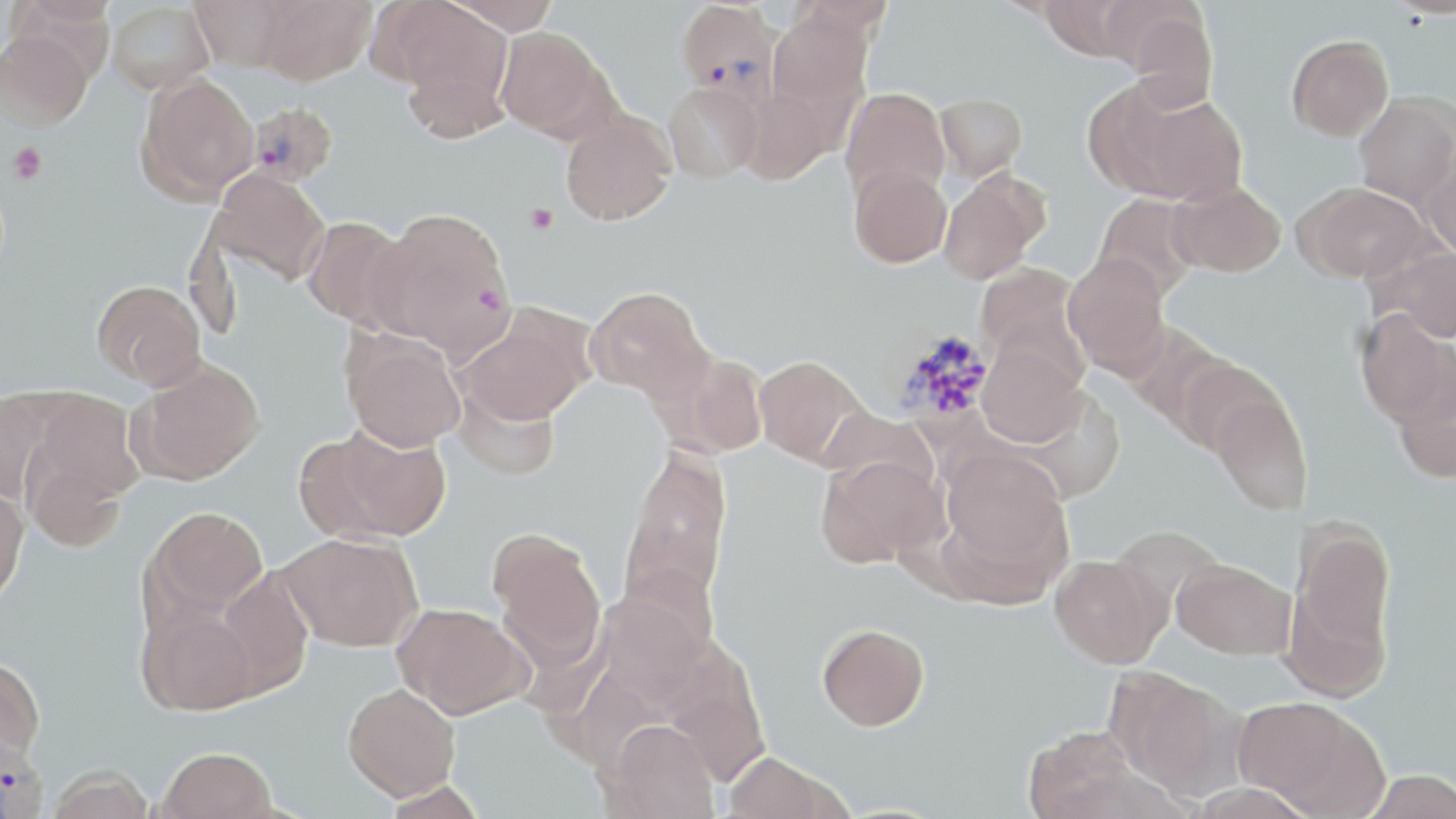
slide_level_diagnosis: Plasmodium vivax
platelet_locations: 'approximate bounding boxes as named x1/y1/x2/y2 corners in pixels: (x1=7, y1=142, x2=47, y2=183), (x1=525, y1=204, x2=558, y2=234)'
magnification: 1000x
plasmodium_vivax_infected_red_blood_cell_locations: 'approximate bounding boxes as named x1/y1/x2/y2 corners in pixels: (x1=676, y1=0, x2=783, y2=101), (x1=246, y1=102, x2=340, y2=187), (x1=886, y1=327, x2=995, y2=431), (x1=0, y1=731, x2=48, y2=818)'
uninfected_red_blood_cell_locations: 'approximate bounding boxes as named x1/y1/x2/y2 corners in pixels: (x1=190, y1=0, x2=295, y2=71), (x1=256, y1=0, x2=376, y2=84), (x1=440, y1=0, x2=560, y2=35), (x1=789, y1=0, x2=895, y2=36), (x1=1038, y1=0, x2=1142, y2=59), (x1=106, y1=2, x2=215, y2=95), (x1=384, y1=2, x2=514, y2=129), (x1=767, y1=5, x2=874, y2=122), (x1=1118, y1=9, x2=1218, y2=111), (x1=494, y1=27, x2=612, y2=139), (x1=0, y1=31, x2=94, y2=130), (x1=1287, y1=35, x2=1393, y2=141), (x1=135, y1=71, x2=260, y2=203), (x1=664, y1=81, x2=764, y2=183), (x1=1095, y1=81, x2=1247, y2=205), (x1=735, y1=87, x2=833, y2=185), (x1=840, y1=88, x2=950, y2=200), (x1=935, y1=93, x2=1027, y2=183), (x1=1354, y1=94, x2=1456, y2=208), (x1=560, y1=110, x2=676, y2=225), (x1=1419, y1=149, x2=1456, y2=259), (x1=849, y1=164, x2=951, y2=268), (x1=208, y1=167, x2=330, y2=286), (x1=938, y1=169, x2=1047, y2=285), (x1=1168, y1=180, x2=1286, y2=277), (x1=1298, y1=182, x2=1428, y2=282), (x1=1092, y1=193, x2=1203, y2=300), (x1=369, y1=207, x2=515, y2=358), (x1=300, y1=216, x2=412, y2=330), (x1=1374, y1=245, x2=1456, y2=342), (x1=1063, y1=253, x2=1172, y2=380), (x1=976, y1=262, x2=1089, y2=373), (x1=92, y1=279, x2=206, y2=390), (x1=585, y1=286, x2=711, y2=401), (x1=457, y1=307, x2=594, y2=425), (x1=1354, y1=309, x2=1454, y2=426), (x1=341, y1=328, x2=465, y2=451), (x1=977, y1=343, x2=1087, y2=448), (x1=658, y1=350, x2=769, y2=458), (x1=754, y1=355, x2=867, y2=466), (x1=132, y1=358, x2=266, y2=485), (x1=1174, y1=358, x2=1284, y2=457), (x1=1393, y1=366, x2=1456, y2=483), (x1=453, y1=380, x2=561, y2=481), (x1=1209, y1=388, x2=1313, y2=515), (x1=0, y1=390, x2=59, y2=504), (x1=22, y1=390, x2=144, y2=516), (x1=820, y1=407, x2=937, y2=495), (x1=299, y1=421, x2=451, y2=544), (x1=22, y1=441, x2=129, y2=553), (x1=620, y1=446, x2=733, y2=614), (x1=936, y1=447, x2=1072, y2=593), (x1=816, y1=454, x2=945, y2=568), (x1=0, y1=485, x2=29, y2=610), (x1=144, y1=506, x2=269, y2=624), (x1=1288, y1=521, x2=1396, y2=681), (x1=490, y1=529, x2=606, y2=672), (x1=278, y1=532, x2=422, y2=651), (x1=1049, y1=554, x2=1167, y2=668), (x1=1172, y1=559, x2=1295, y2=659), (x1=212, y1=568, x2=315, y2=699), (x1=590, y1=589, x2=708, y2=710), (x1=393, y1=603, x2=533, y2=719), (x1=138, y1=605, x2=259, y2=714), (x1=817, y1=623, x2=930, y2=731), (x1=659, y1=640, x2=771, y2=787), (x1=0, y1=655, x2=46, y2=765), (x1=1104, y1=667, x2=1242, y2=799), (x1=342, y1=683, x2=460, y2=801), (x1=1231, y1=696, x2=1376, y2=814), (x1=602, y1=719, x2=720, y2=819), (x1=1024, y1=725, x2=1146, y2=819), (x1=156, y1=747, x2=278, y2=819), (x1=722, y1=751, x2=846, y2=818), (x1=44, y1=764, x2=155, y2=819), (x1=1361, y1=769, x2=1456, y2=818)'
image_size: 1456×819 pixels
modality: optical microscopy
field_of_view: one of a larger specimen
stain: May-Grünwald-Giemsa
preparation: thin blood smear